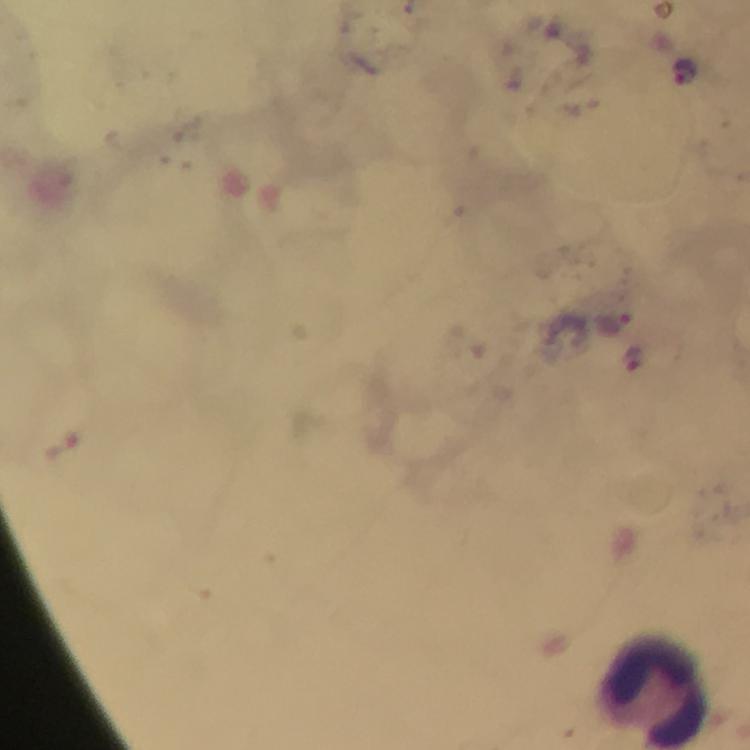

leukocyte_locations: 'approximate centers as {x, y} in pixels: {651, 692}'
preparation: thick blood film
image_size: 750×750 pixels
malaria_parasite_locations: 'approximate centers as {x, y} in pixels: {687, 72}, {616, 325}, {633, 359}, {62, 444}'
immersion_oil: used
stain: Giemsa
capture: smartphone photograph through a microscope
context: from a diagnostic examination for malaria
cropped_from: a single field of view
magnification: 100x